Locate every Plasmodium parasite.
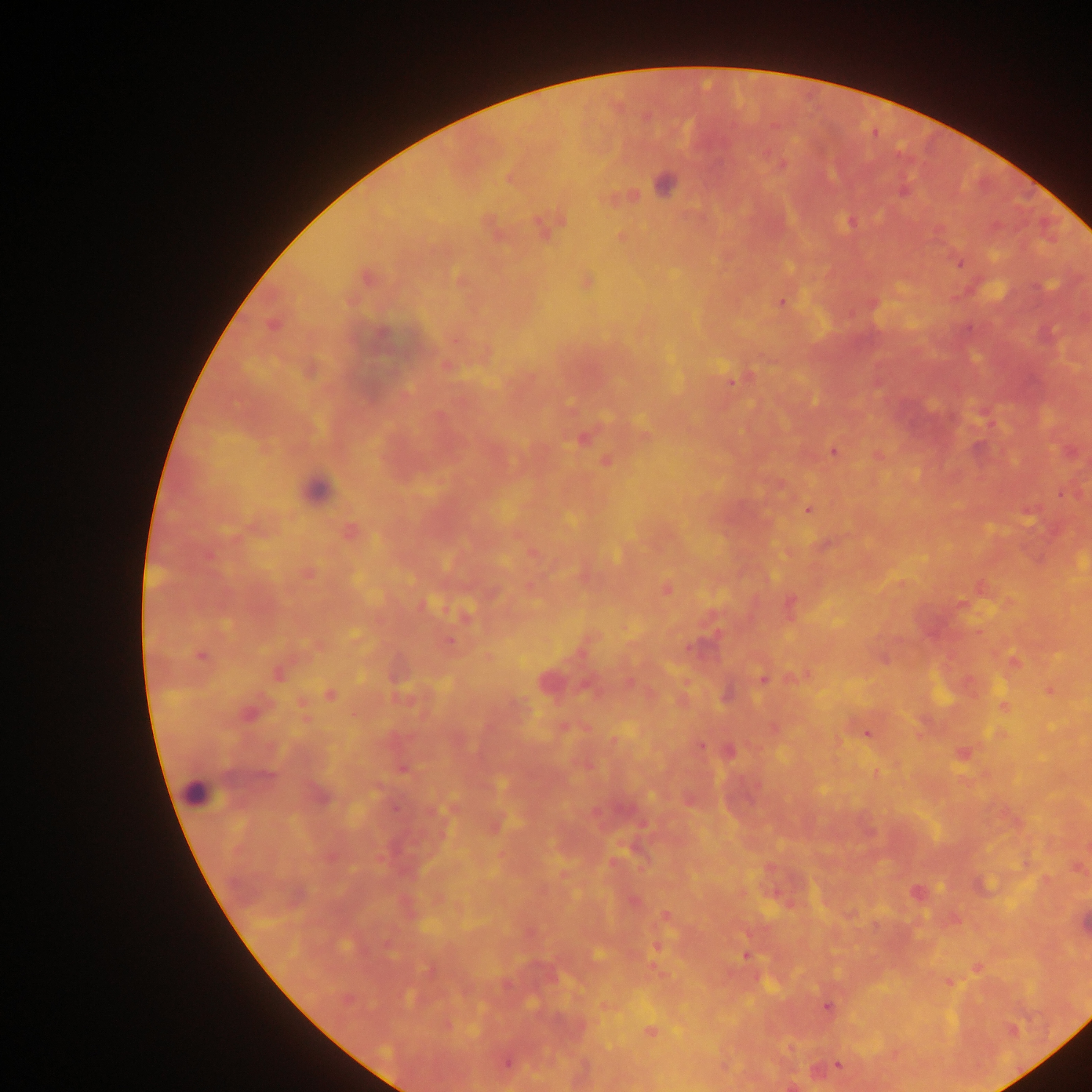
Approximate centers as (x, y) in pixels.
Plasmodium parasites: (782, 165), (510, 179), (664, 185), (903, 193), (850, 222), (542, 226), (959, 263), (367, 277), (781, 302), (273, 326), (731, 381), (582, 440), (833, 451), (606, 461), (808, 510), (349, 531), (309, 575), (666, 589), (425, 604), (962, 605), (449, 642), (691, 648), (200, 656), (1014, 660), (278, 674), (762, 679), (547, 681), (1050, 690), (330, 695), (1004, 705), (248, 714), (867, 734), (700, 746), (729, 751), (962, 754), (403, 770), (917, 891), (634, 902), (665, 915), (598, 955), (745, 956), (950, 984), (828, 1007), (650, 1031), (1013, 1031), (506, 1064), (838, 1065).

capture = mobile-phone photograph through a microscope
image size = 1092×1092 pixels
leukocyte locations = approximate centers as (x, y) in pixels: (316, 488), (194, 793)
field of view = single
preparation = thick blood smear
country = Ghana